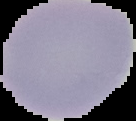
Summary:
  - Preparation: thin blood smear
  - Image type: segmented cell region on a black background
  - Result: no Plasmodium parasites seen
  - Image size: 136×121 pixels